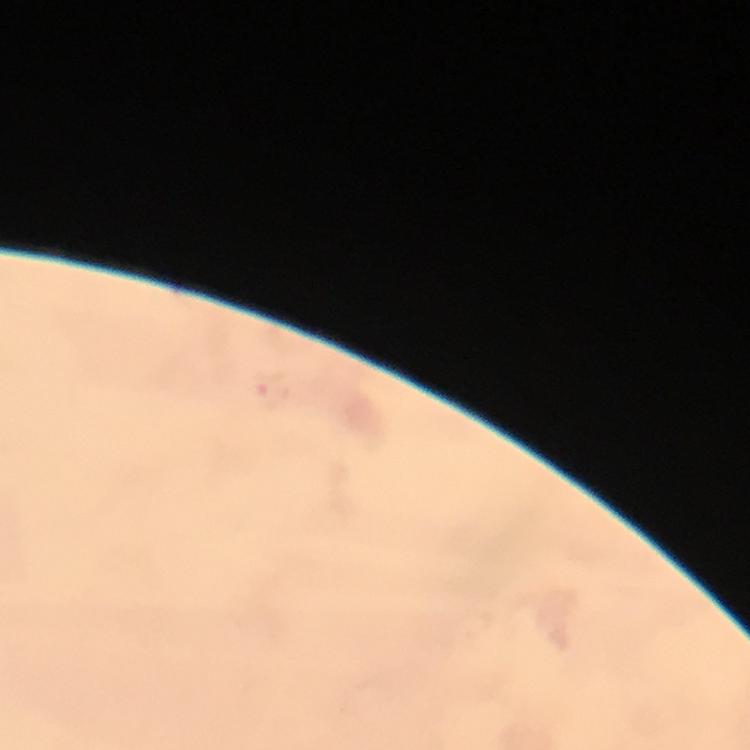
Approximate centers as (x, y) in pixels. Malaria parasite locations: (269, 390). A crop from one field of view. Thick smear. Immersion oil was used. Giemsa stain. At 100x magnification. Smartphone photograph taken through a microscope. Image is 750×750 pixels. From a malaria diagnostic workup.